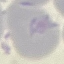
malaria_status: uninfected
capture: smartphone through the microscope eyepiece
preparation: thin smear
image_type: automatically extracted cell patch, resized to 64 × 64 pixels
stain: Giemsa